Assess the morphology of the red blood cells.
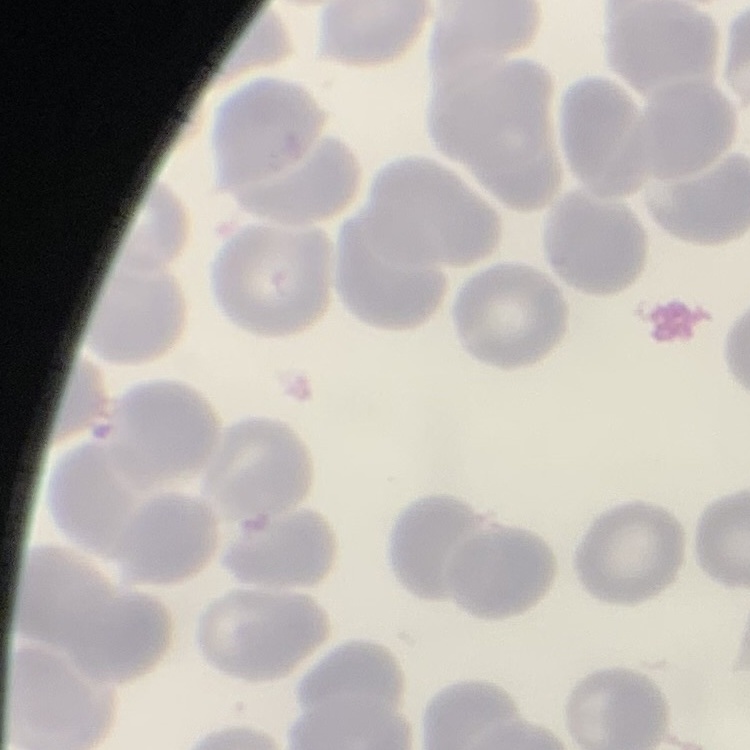

They show no rouleaux formation.

Summary:
  - Preparation: thin peripheral smear
  - Stain: Field's or Giemsa
  - Image type: square crop of a larger photomicrograph